Locate and identify every blood parasite.
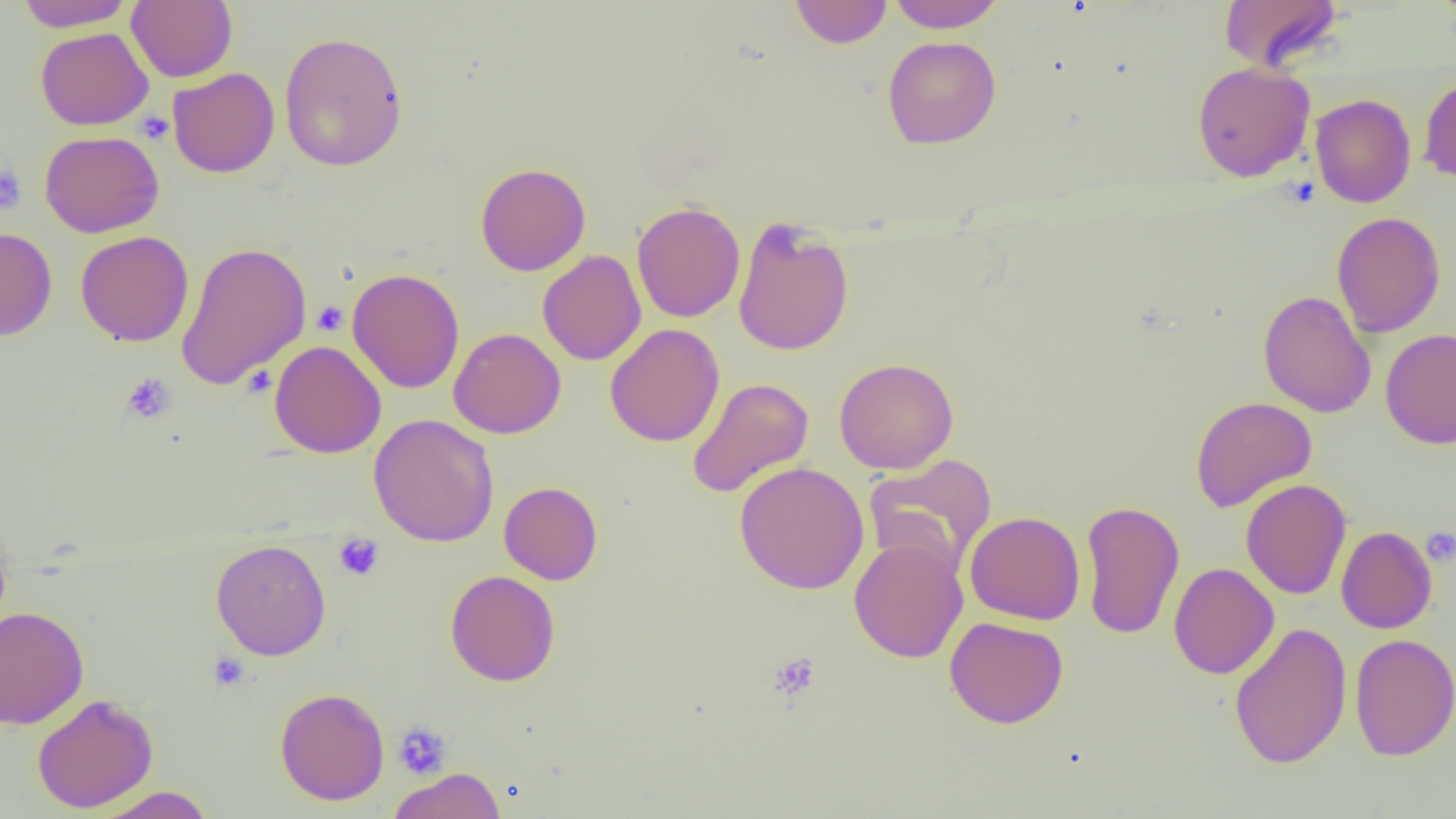
No blood parasites observed.

slide_level_diagnosis: negative for blood parasites
modality: optical microscopy
field_of_view: single
uninfected_red_blood_cell_locations: 'approximate bounding boxes as (x1, y1, x2, y2) in pixels: (15, 0, 133, 30), (790, 0, 892, 48), (886, 0, 1004, 32), (1218, 0, 1344, 73), (127, 1, 237, 82), (35, 27, 153, 130), (278, 31, 408, 172), (882, 36, 1001, 149), (1192, 62, 1315, 182), (167, 67, 279, 178), (1419, 76, 1456, 186), (1310, 93, 1416, 208), (39, 130, 165, 238), (475, 162, 591, 275), (631, 201, 746, 323), (1331, 212, 1446, 337), (732, 217, 854, 356), (0, 227, 57, 341), (76, 231, 194, 347), (176, 241, 311, 389), (537, 250, 647, 366), (347, 267, 465, 394), (1258, 290, 1376, 418), (605, 323, 724, 447), (449, 328, 566, 439), (1380, 329, 1456, 449), (269, 340, 386, 458), (833, 357, 959, 474), (686, 377, 814, 499), (1190, 396, 1317, 513), (368, 414, 499, 547), (863, 453, 997, 576), (733, 462, 870, 594), (1241, 479, 1351, 600), (499, 481, 603, 584), (1080, 499, 1185, 640), (964, 511, 1085, 625), (1336, 526, 1437, 634), (849, 537, 968, 663), (211, 538, 331, 660), (1169, 562, 1279, 679), (445, 570, 560, 686), (0, 606, 88, 729), (945, 616, 1069, 728), (1228, 621, 1352, 769), (1350, 633, 1456, 761), (275, 687, 390, 806), (31, 694, 158, 813), (388, 768, 505, 819), (94, 786, 215, 818)'
magnification: 1000x
platelet_locations: 'approximate bounding boxes as (x1, y1, x2, y2) in pixels: (136, 110, 174, 143), (0, 164, 27, 214), (312, 301, 348, 336), (121, 372, 176, 424), (1421, 527, 1456, 567), (333, 533, 384, 580), (208, 652, 250, 691), (767, 652, 822, 702), (392, 721, 452, 780)'
preparation: thin blood film
image_size: 1456×819 pixels